Point out every Plasmodium parasite.
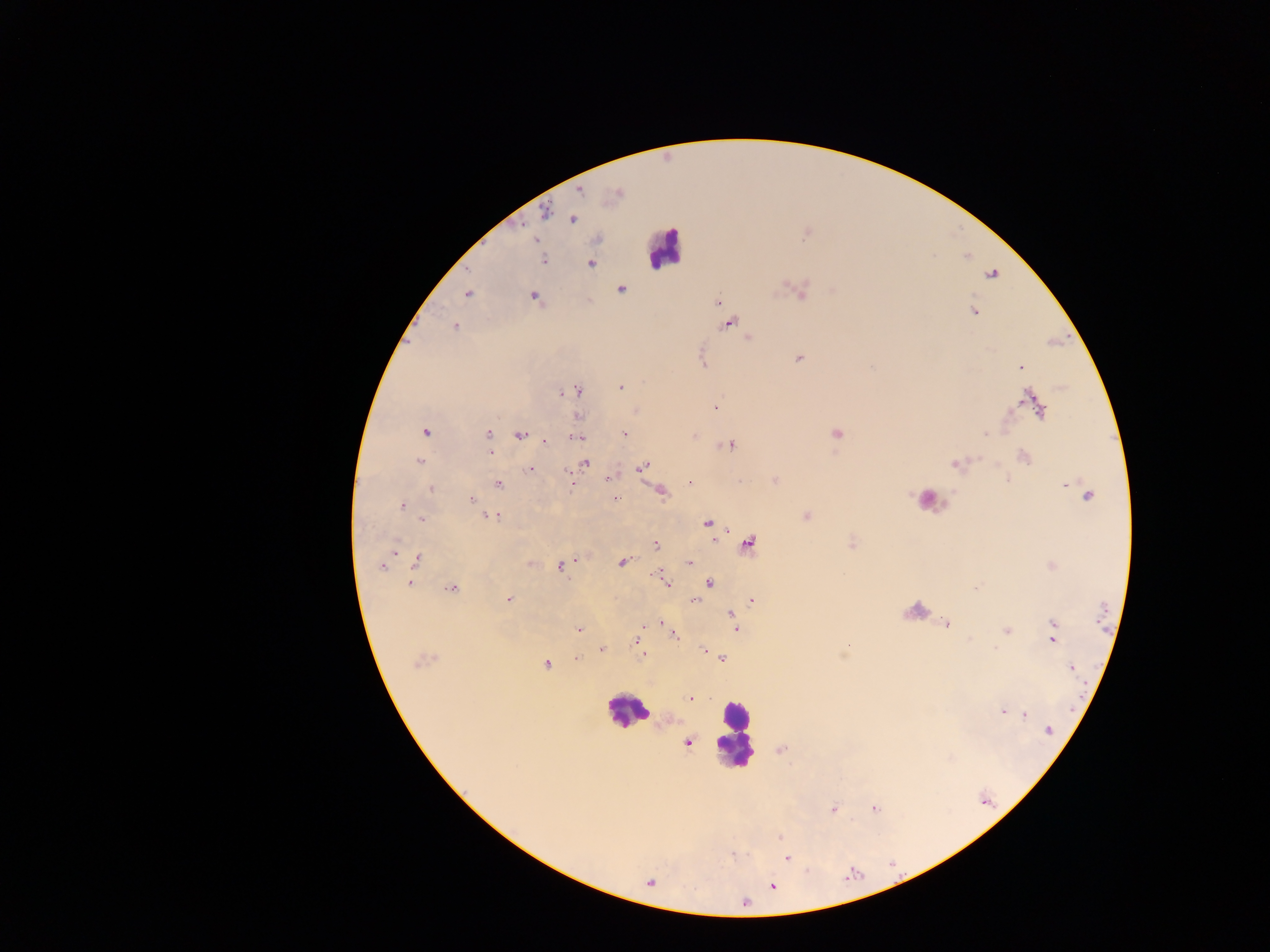

Approximate centers as (x, y) in pixels.
Plasmodium parasites (some below the resolvable threshold): (572, 220), (806, 236), (598, 240), (535, 241), (543, 260), (592, 265), (622, 290), (468, 294), (534, 295), (717, 302), (973, 312), (730, 323), (455, 326), (749, 337), (798, 358), (702, 362), (1020, 368), (622, 388), (576, 391), (560, 393), (1038, 404), (716, 405), (425, 432), (624, 433), (487, 435), (695, 435), (987, 435), (519, 436), (574, 438), (545, 443), (732, 446), (488, 453), (420, 462), (586, 464), (641, 466), (529, 469), (565, 473), (690, 481), (497, 484), (432, 488), (1088, 494), (472, 499), (615, 499), (402, 506), (493, 516), (489, 518), (498, 518), (421, 519), (707, 522), (749, 543), (656, 545), (394, 549), (416, 559), (577, 559), (622, 563), (689, 563), (384, 567), (561, 568), (657, 576), (664, 579), (409, 582), (709, 582), (451, 588), (510, 598), (751, 599), (695, 600), (729, 614), (660, 622), (946, 623), (579, 629), (736, 629), (1005, 630), (1054, 631), (674, 635), (635, 642), (994, 647), (702, 649), (603, 650), (642, 656), (723, 658), (577, 659), (419, 660), (546, 663), (1072, 668), (690, 698), (1004, 711), (1026, 714), (1050, 730), (687, 741), (876, 808), (834, 809), (780, 837), (735, 855), (787, 859), (772, 886).

Leukocyte locations: (664, 247), (625, 715), (737, 731). Photographed through a microscope with a mobile-phone camera. Image is 1270×952 pixels. Collected in Ghana. Thick blood film. Single field of view.